Report the malaria status of this cell.
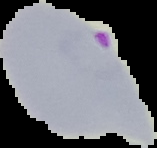

It is parasitized.

Summary:
  - Image type: segmented cell region with the area outside set to black
  - Preparation: thin blood film
  - Image size: 157×148 pixels